Locate and identify every blood parasite.
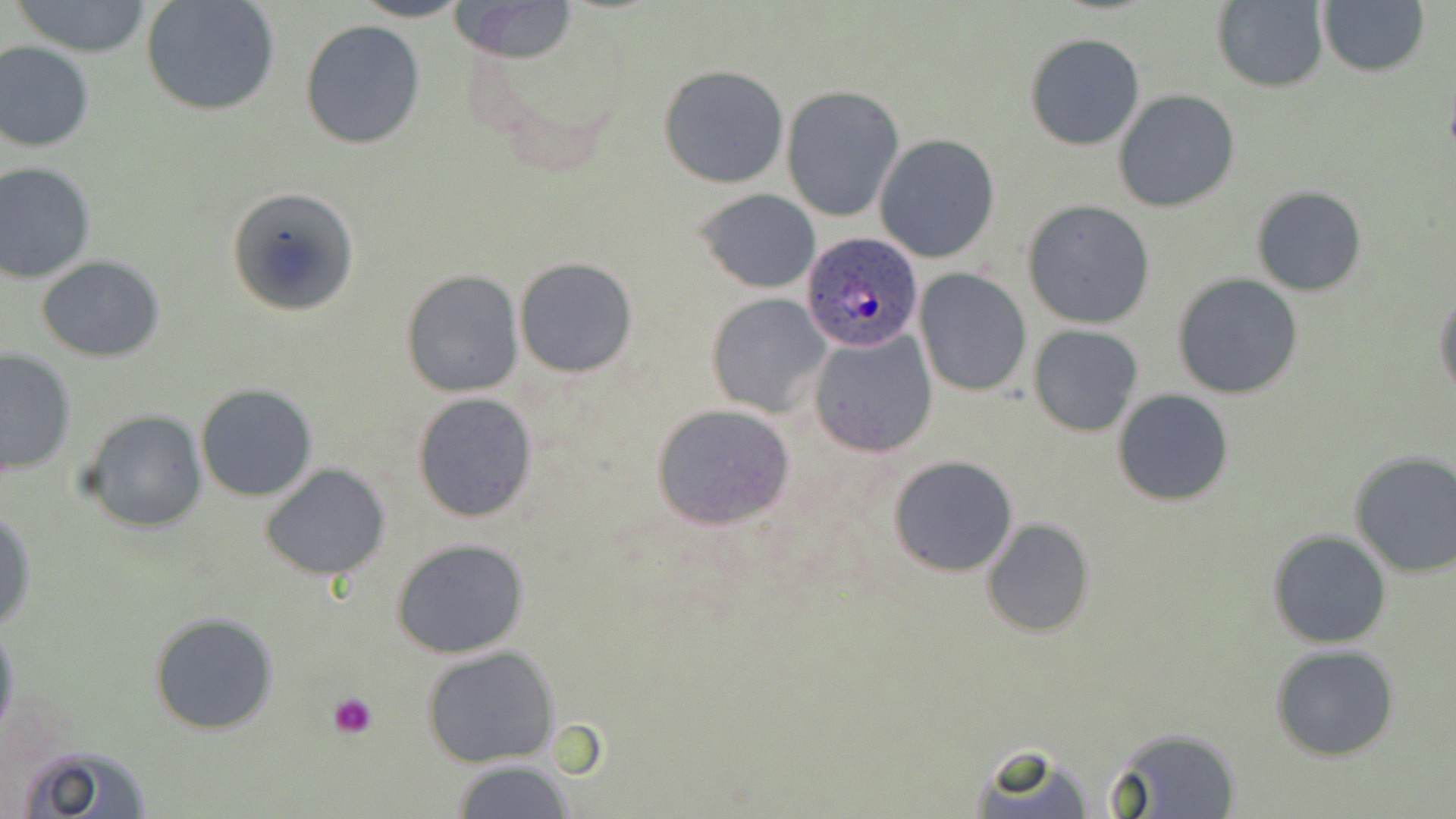
Approximate bounding boxes as (x1, y1, x2, y2) in pixels.
Plasmodium ovale-infected red blood cells: (802, 231, 923, 352).
No Plasmodium falciparum, Plasmodium malariae, Plasmodium vivax, Babesia divergens, or Trypanosoma brucei observed.

Summary:
  - Platelet locations: (327, 691, 380, 738)
  - Uninfected red blood cell locations: (7, 0, 156, 58), (141, 0, 281, 117), (351, 0, 470, 22), (449, 0, 579, 62), (1211, 1, 1330, 92), (1319, 1, 1429, 77), (300, 18, 427, 149), (1025, 34, 1145, 150), (0, 40, 94, 153), (658, 64, 790, 189), (781, 86, 904, 222), (1112, 90, 1241, 212), (875, 135, 1000, 263), (0, 163, 97, 283), (1251, 186, 1366, 296), (228, 187, 360, 319), (695, 189, 822, 293), (1021, 198, 1155, 329), (35, 255, 165, 362), (514, 257, 639, 377), (914, 270, 1032, 396), (400, 271, 524, 397), (1172, 272, 1304, 399), (1434, 291, 1456, 402), (706, 293, 831, 417), (1028, 325, 1144, 436), (808, 330, 938, 458), (0, 348, 76, 478), (194, 382, 318, 503), (1113, 389, 1235, 507), (412, 391, 539, 525), (650, 403, 795, 531), (79, 410, 208, 533), (1348, 452, 1456, 578), (887, 454, 1019, 576), (260, 463, 393, 582), (0, 510, 37, 633), (982, 519, 1095, 636), (1267, 530, 1391, 648), (389, 538, 532, 659), (149, 612, 279, 735), (0, 619, 20, 747), (1270, 643, 1399, 761), (422, 646, 563, 769), (1101, 729, 1241, 818), (17, 743, 152, 819), (963, 746, 1098, 818), (449, 760, 577, 819)
  - Slide-level diagnosis: Plasmodium ovale
  - Preparation: thin blood film
  - Field of view: single
  - Modality: light microscopy
  - Image size: 1456×819 pixels
  - Stain: May-Grünwald-Giemsa
  - Magnification: 1000x